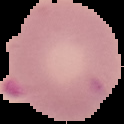
Summary:
  - Preparation: thin blood smear
  - Result: malaria parasites identified
  - Image size: 124×124 pixels
  - Image type: segmented cell region on a black background